Assess this cell for malaria.
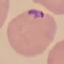

Parasitized.

Cell patch, automatically extracted from a larger field of view and resized to 64 × 64 pixels. Thin smear of blood. Giemsa stain. Acquired by smartphone through the microscope eyepiece.